Report the malaria status.
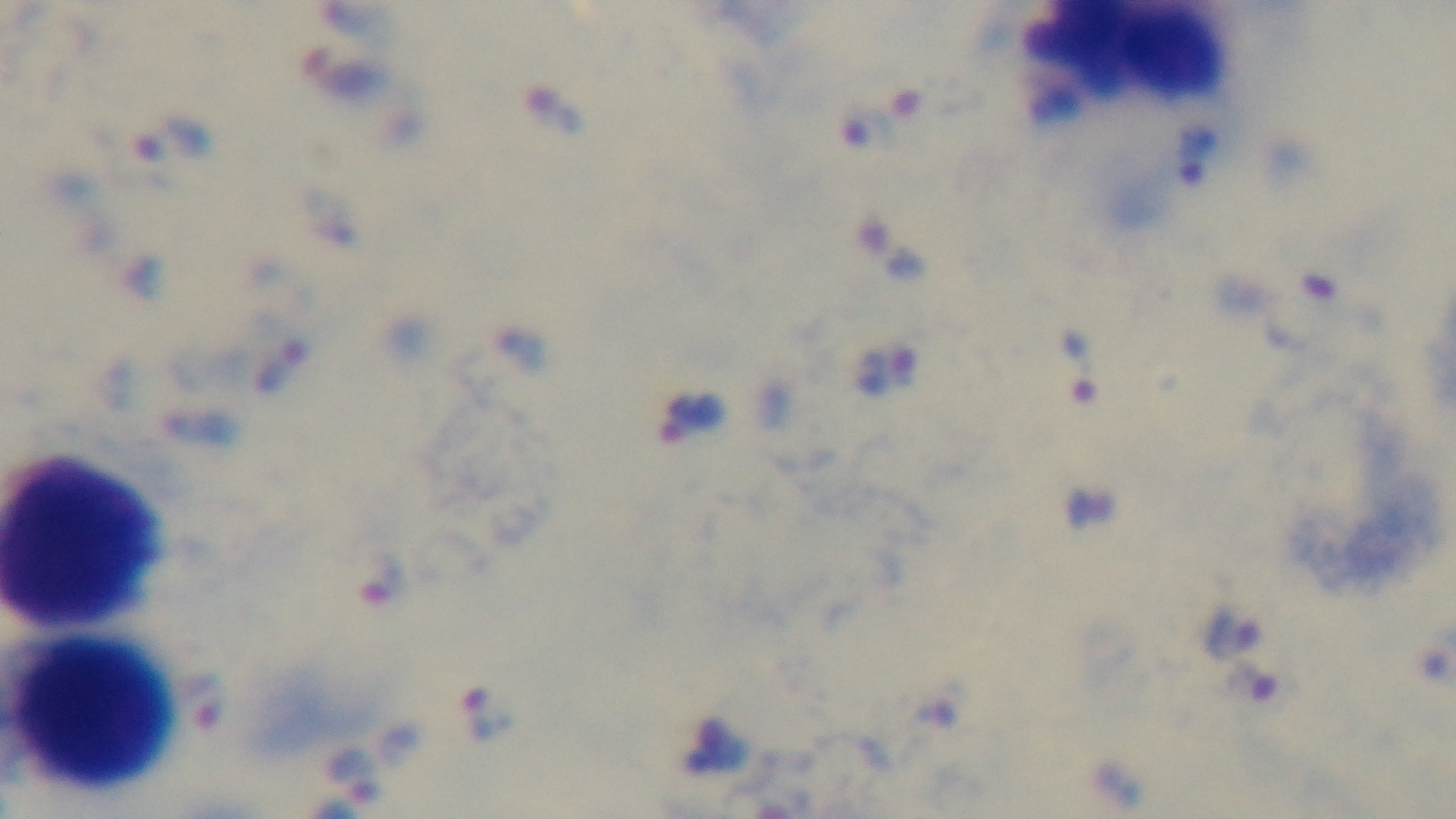

It is infected.

{
  "preparation": "thick smear",
  "capture": "mounted 4K digital camera",
  "field_of_view": "one from the slide",
  "stain": "Giemsa",
  "modality": "light microscopy",
  "objective": "100x oil immersion"
}